Comment on the morphology of the erythrocytes.
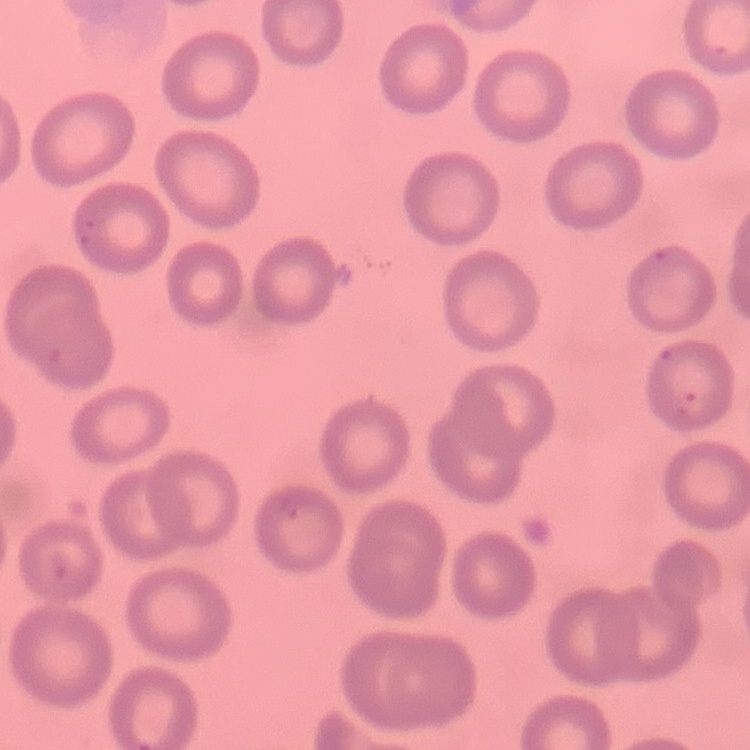
No rouleaux formation.

One tile cut from a larger photomicrograph. Stained with either Field's or Giemsa. Thin blood film.